Identify the parasite.
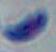

Toxoplasma gondii.

Summary:
  - Magnification: 1000x
  - Modality: photomicrograph